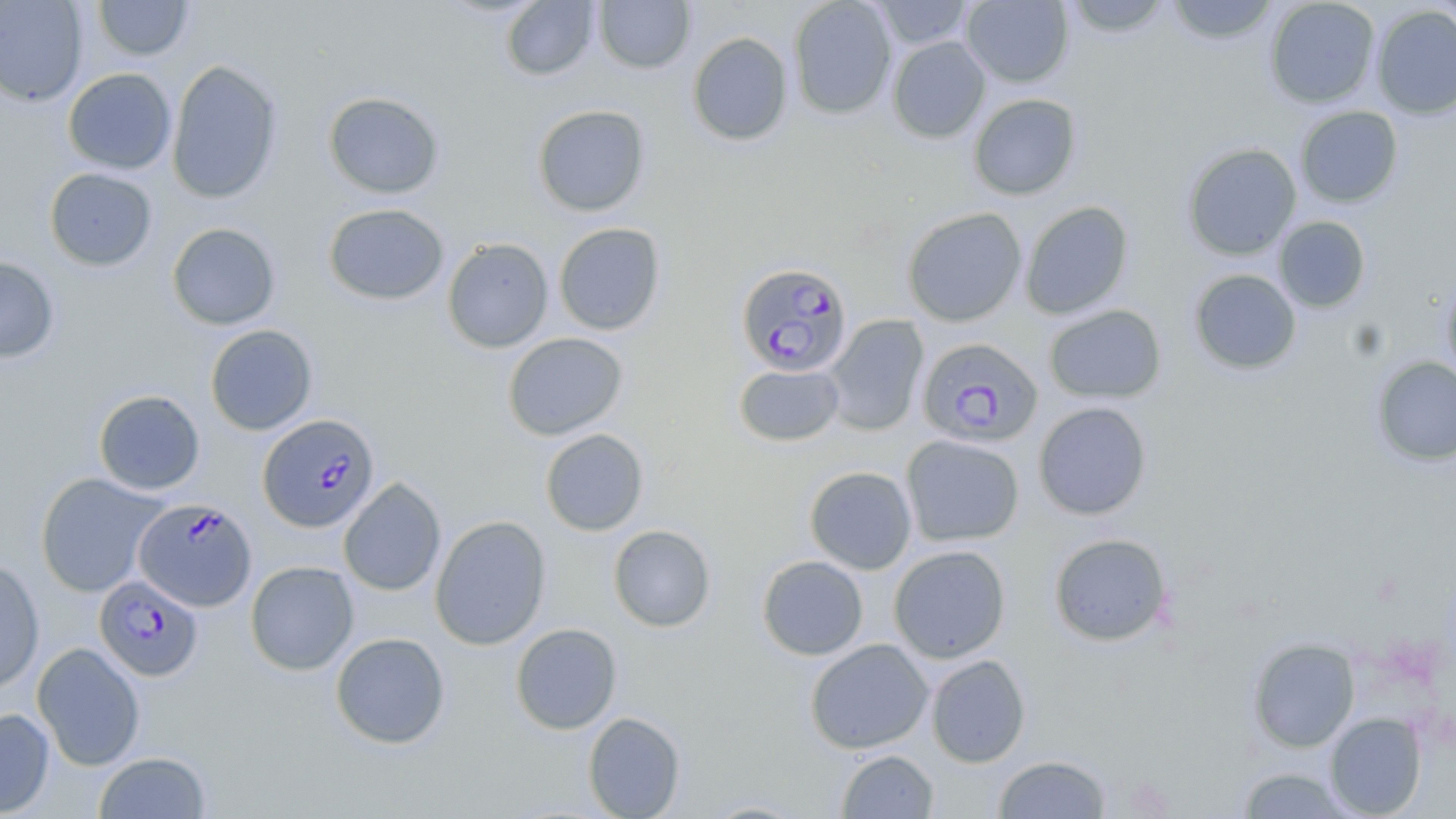
Approximate bounding boxes as [x1, y1, x2, y2] in pixels. Plasmodium falciparum-infected red blood cell locations: [736, 262, 852, 378], [916, 337, 1043, 448], [257, 414, 381, 532], [134, 497, 257, 612], [94, 575, 203, 682]. Uninfected red blood cell locations: [0, 0, 88, 106], [92, 0, 195, 61], [593, 0, 695, 74], [788, 0, 897, 119], [870, 0, 975, 50], [961, 0, 1074, 88], [1062, 0, 1173, 38], [1164, 0, 1280, 45], [1264, 0, 1380, 108], [1429, 0, 1456, 35], [500, 1, 600, 81], [1371, 5, 1456, 120], [687, 31, 794, 146], [887, 36, 990, 143], [166, 59, 284, 204], [63, 68, 177, 175], [323, 91, 445, 199], [968, 93, 1082, 200], [532, 104, 651, 217], [1295, 106, 1403, 208], [1181, 143, 1302, 260], [44, 167, 158, 271], [1020, 200, 1134, 320], [323, 203, 449, 305], [902, 207, 1027, 327], [1273, 216, 1371, 313], [167, 222, 281, 330], [553, 222, 666, 335], [442, 237, 554, 353], [0, 256, 60, 363], [1188, 269, 1302, 375], [1440, 270, 1456, 386], [1044, 304, 1167, 404], [823, 314, 929, 436], [204, 324, 318, 435], [503, 332, 628, 441], [1371, 356, 1456, 466], [734, 363, 843, 446], [93, 389, 205, 495], [1033, 401, 1152, 520], [540, 429, 649, 536], [901, 434, 1024, 547], [804, 466, 917, 574], [35, 472, 168, 597], [338, 477, 446, 596], [430, 515, 551, 650], [608, 524, 716, 632], [1049, 533, 1172, 646], [888, 544, 1012, 663], [757, 555, 869, 660], [0, 556, 45, 694], [245, 560, 359, 676], [510, 623, 622, 734], [330, 632, 451, 749], [1248, 637, 1360, 752], [805, 639, 933, 754], [32, 642, 146, 771], [925, 654, 1030, 768], [0, 707, 55, 817], [582, 711, 686, 819], [1324, 712, 1427, 818], [836, 749, 939, 818], [93, 751, 212, 818], [993, 754, 1112, 818], [1237, 766, 1358, 818], [698, 799, 812, 818]. Slide-level diagnosis: Plasmodium falciparum. 1000x magnification. Light microscopy. May-Grünwald-Giemsa-stained preparation. One field of a larger specimen. Thin blood film. Image is 1456×819 pixels.